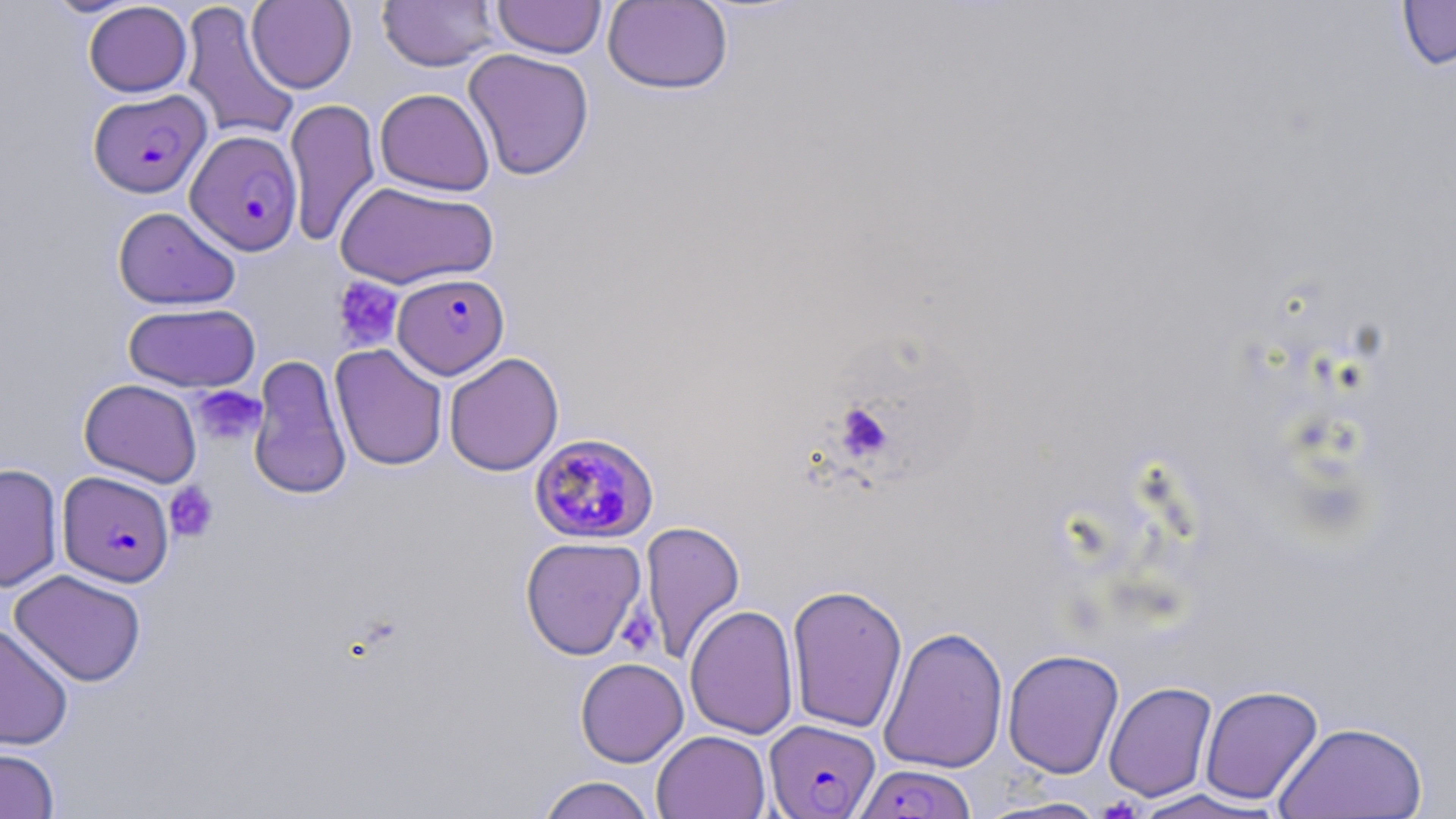
Approximate bounding boxes as (x1, y1, x2, y2) in pixels. Platelet locations: (331, 276, 403, 351), (192, 385, 265, 446), (835, 402, 893, 460), (164, 482, 219, 542), (616, 603, 660, 657). Plasmodium falciparum-infected red blood cell locations: (88, 89, 212, 199), (185, 130, 303, 255), (398, 271, 511, 375), (528, 433, 660, 545), (58, 471, 174, 587), (763, 718, 881, 818), (855, 763, 976, 819). Uninfected red blood cell locations: (43, 0, 142, 17), (246, 0, 357, 93), (377, 0, 501, 71), (492, 0, 607, 59), (1395, 0, 1456, 72), (179, 1, 300, 143), (602, 1, 734, 95), (83, 2, 192, 97), (463, 48, 595, 181), (375, 88, 495, 195), (284, 98, 381, 247), (334, 180, 499, 290), (113, 206, 240, 310), (123, 302, 261, 393), (330, 344, 448, 471), (443, 352, 564, 477), (248, 354, 352, 501), (79, 379, 202, 487), (0, 463, 64, 593), (641, 521, 745, 663), (520, 536, 646, 660), (9, 569, 147, 687), (786, 583, 909, 734), (684, 604, 800, 739), (0, 622, 74, 750), (878, 626, 1009, 774), (1002, 648, 1124, 779), (575, 657, 689, 767), (1103, 681, 1218, 802), (1199, 684, 1323, 806), (1274, 720, 1429, 818), (652, 730, 771, 819), (0, 745, 60, 818), (536, 775, 657, 819), (1128, 789, 1283, 818), (976, 796, 1114, 818). Slide-level diagnosis: Plasmodium falciparum. Optical microscopy. May-Grünwald-Giemsa-stained preparation. Image is 1456×819 pixels. 1000x magnification. Single field of view. Thin blood smear.